Identify the blood parasite species.
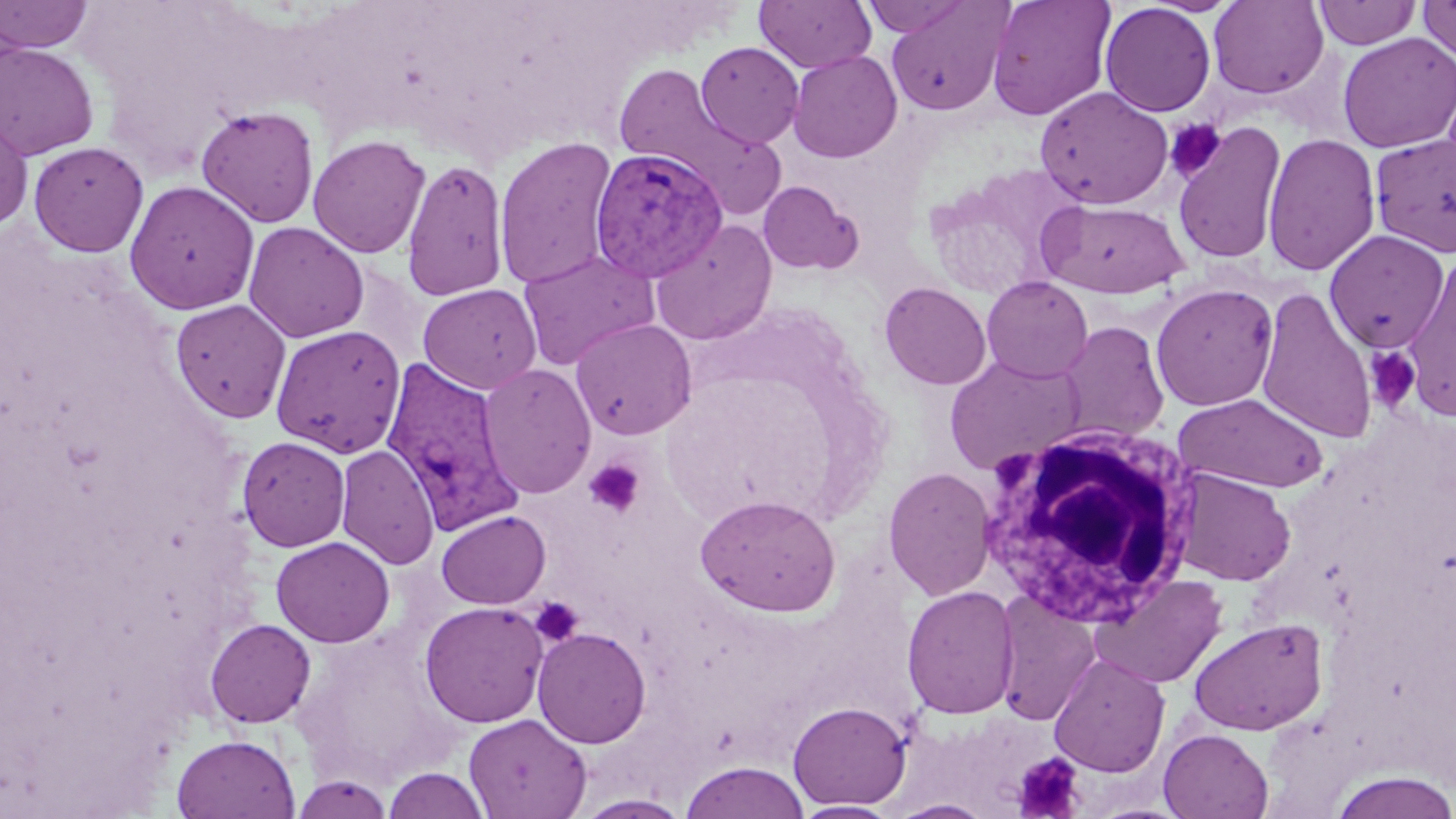

Plasmodium vivax.

Summary:
  - Coordinate format: approximate bounding boxes as [x1, y1, x2, y2] in pixels
  - Uninfected red blood cell locations: [0, 0, 93, 54], [755, 0, 876, 73], [861, 0, 972, 37], [986, 0, 1116, 121], [1418, 0, 1456, 64], [886, 1, 1012, 116], [1209, 1, 1328, 99], [1313, 1, 1421, 49], [1100, 2, 1216, 116], [1337, 32, 1456, 153], [696, 41, 804, 148], [0, 42, 100, 160], [787, 50, 902, 163], [611, 61, 756, 188], [1034, 86, 1173, 210], [196, 105, 320, 227], [645, 105, 790, 219], [0, 114, 33, 231], [1171, 120, 1287, 265], [1262, 132, 1381, 276], [1369, 132, 1456, 257], [308, 135, 431, 258], [493, 136, 618, 289], [28, 140, 149, 257], [401, 158, 510, 301], [124, 180, 260, 315], [757, 180, 862, 275], [1038, 198, 1190, 299], [650, 220, 777, 346], [243, 221, 369, 343], [1325, 229, 1448, 352], [518, 250, 658, 370], [1403, 254, 1456, 422], [343, 263, 428, 367], [981, 275, 1093, 382], [879, 281, 992, 390], [418, 283, 542, 394], [1150, 283, 1279, 411], [1255, 286, 1377, 444], [170, 299, 291, 423], [570, 317, 697, 440], [1057, 321, 1170, 443], [271, 325, 406, 458], [944, 354, 1086, 475], [478, 363, 596, 498], [1173, 393, 1329, 493], [237, 436, 350, 551], [336, 444, 439, 570], [882, 466, 997, 601], [1171, 468, 1296, 586], [695, 494, 841, 617], [436, 510, 550, 609], [271, 536, 395, 647], [1090, 574, 1228, 689], [902, 585, 1019, 719], [994, 591, 1101, 725], [420, 601, 548, 728], [1188, 616, 1329, 735], [204, 618, 316, 728], [532, 627, 652, 748], [1049, 653, 1170, 777], [787, 701, 912, 810], [463, 713, 591, 818], [1158, 729, 1273, 818], [171, 733, 300, 818], [681, 761, 810, 819], [383, 767, 491, 818], [1329, 771, 1456, 818], [291, 773, 393, 817], [574, 794, 693, 818], [887, 799, 994, 818], [791, 801, 900, 819]
  - White blood cell locations: [977, 422, 1201, 626]
  - Plasmodium vivax-infected red blood cell locations: [589, 147, 729, 283], [381, 356, 524, 535]
  - Platelet locations: [1165, 118, 1227, 182], [1364, 347, 1422, 413], [583, 459, 645, 518], [531, 597, 583, 646], [1013, 753, 1085, 817]
  - Preparation: thin blood film
  - Image size: 1456×819 pixels
  - Modality: optical microscopy
  - Magnification: 1000x
  - Field of view: one of a larger specimen
  - Stain: May-Grünwald-Giemsa